Identify the blood parasite species.
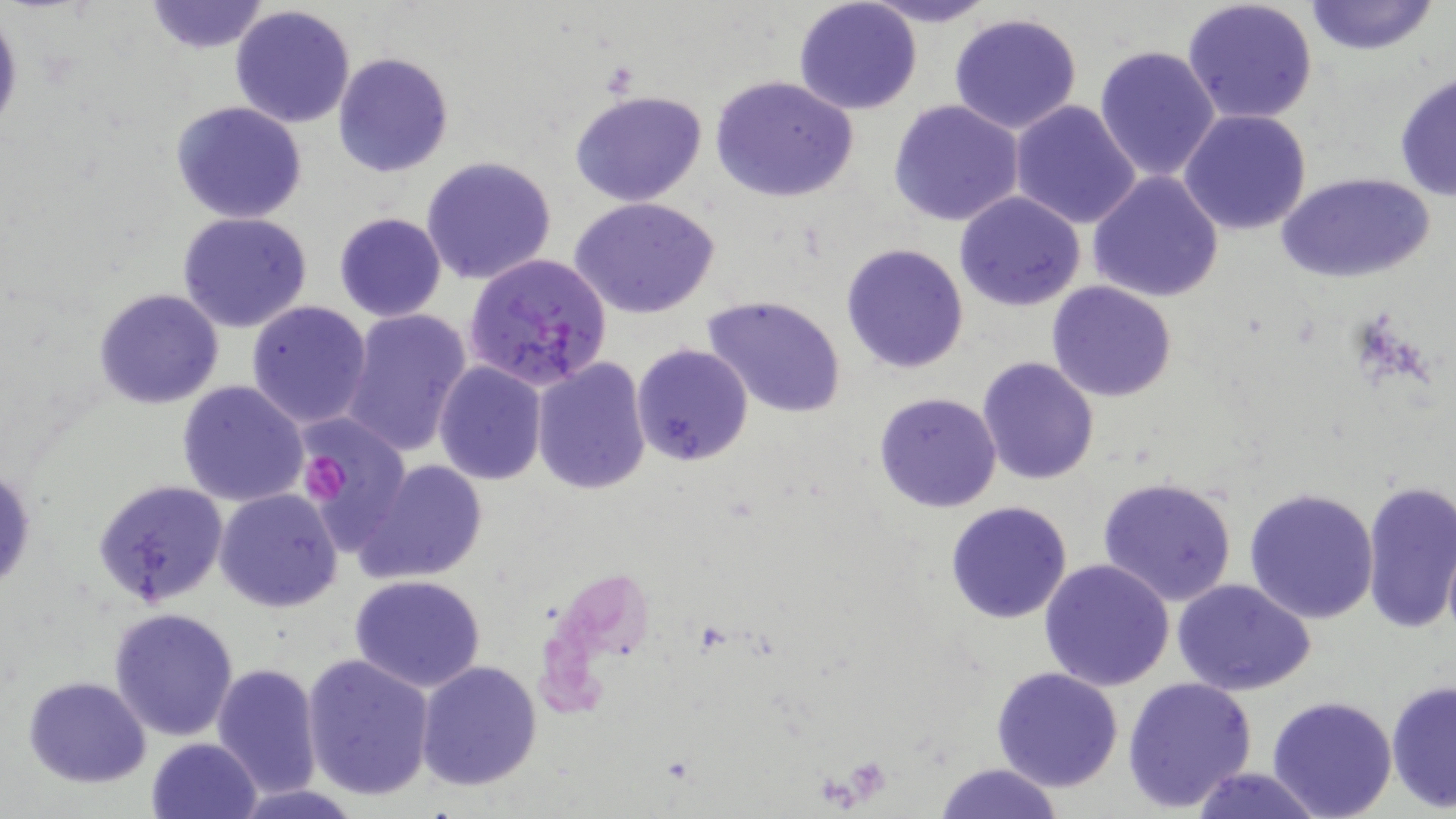

Plasmodium falciparum.

Summary:
  - Coordinate format: approximate bounding boxes as named x1/y1/x2/y2 corners in pixels
  - Uninfected red blood cell locations: (x1=144, y1=0, x2=270, y2=54), (x1=860, y1=0, x2=1001, y2=27), (x1=1183, y1=0, x2=1318, y2=125), (x1=1304, y1=0, x2=1440, y2=56), (x1=793, y1=2, x2=923, y2=115), (x1=229, y1=4, x2=357, y2=128), (x1=0, y1=7, x2=23, y2=142), (x1=948, y1=13, x2=1083, y2=136), (x1=1093, y1=43, x2=1221, y2=183), (x1=333, y1=51, x2=453, y2=177), (x1=1392, y1=70, x2=1455, y2=201), (x1=709, y1=75, x2=859, y2=204), (x1=570, y1=90, x2=709, y2=206), (x1=888, y1=99, x2=1025, y2=227), (x1=1009, y1=99, x2=1142, y2=229), (x1=170, y1=101, x2=309, y2=223), (x1=1178, y1=109, x2=1313, y2=234), (x1=421, y1=156, x2=557, y2=285), (x1=1279, y1=170, x2=1435, y2=284), (x1=1087, y1=171, x2=1225, y2=303), (x1=955, y1=191, x2=1087, y2=312), (x1=571, y1=197, x2=720, y2=319), (x1=177, y1=212, x2=312, y2=333), (x1=333, y1=212, x2=447, y2=321), (x1=840, y1=243, x2=968, y2=374), (x1=1046, y1=282, x2=1176, y2=402), (x1=93, y1=288, x2=223, y2=410), (x1=701, y1=295, x2=847, y2=421), (x1=245, y1=300, x2=374, y2=429), (x1=339, y1=308, x2=473, y2=456), (x1=631, y1=343, x2=754, y2=466), (x1=976, y1=356, x2=1101, y2=485), (x1=531, y1=358, x2=652, y2=494), (x1=433, y1=361, x2=547, y2=484), (x1=175, y1=380, x2=309, y2=506), (x1=873, y1=392, x2=1002, y2=512), (x1=296, y1=418, x2=412, y2=552), (x1=355, y1=459, x2=488, y2=585), (x1=0, y1=464, x2=37, y2=597), (x1=1097, y1=475, x2=1239, y2=608), (x1=1360, y1=478, x2=1456, y2=634), (x1=93, y1=480, x2=229, y2=610), (x1=214, y1=487, x2=343, y2=613), (x1=1243, y1=487, x2=1378, y2=624), (x1=945, y1=501, x2=1073, y2=623), (x1=1441, y1=534, x2=1456, y2=640), (x1=1037, y1=558, x2=1175, y2=689), (x1=348, y1=574, x2=486, y2=692), (x1=1172, y1=580, x2=1317, y2=696), (x1=108, y1=606, x2=240, y2=741), (x1=302, y1=653, x2=436, y2=800), (x1=415, y1=659, x2=544, y2=791), (x1=211, y1=661, x2=323, y2=797), (x1=991, y1=667, x2=1124, y2=793), (x1=23, y1=675, x2=150, y2=787), (x1=1122, y1=675, x2=1258, y2=813), (x1=1386, y1=679, x2=1455, y2=815), (x1=1265, y1=695, x2=1397, y2=819), (x1=147, y1=737, x2=262, y2=819), (x1=933, y1=762, x2=1064, y2=819), (x1=1188, y1=766, x2=1324, y2=819), (x1=230, y1=784, x2=368, y2=819)
  - Platelet locations: (x1=300, y1=454, x2=349, y2=499)
  - Plasmodium falciparum-infected red blood cell locations: (x1=463, y1=253, x2=614, y2=392)
  - Modality: optical microscopy
  - Image size: 1456×819 pixels
  - Magnification: 1000x
  - Stain: May-Grünwald-Giemsa
  - Field of view: single
  - Preparation: thin blood film